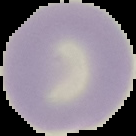 Image is 136×136 pixels. From a thin blood smear. Malaria status: uninfected. Cell region segmented out of the field of view; the surrounding area is masked to black.